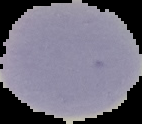

image_size: 142×124 pixels
image_type: segmented cell region on a black background
result: negative for Plasmodium parasites
preparation: thin blood smear